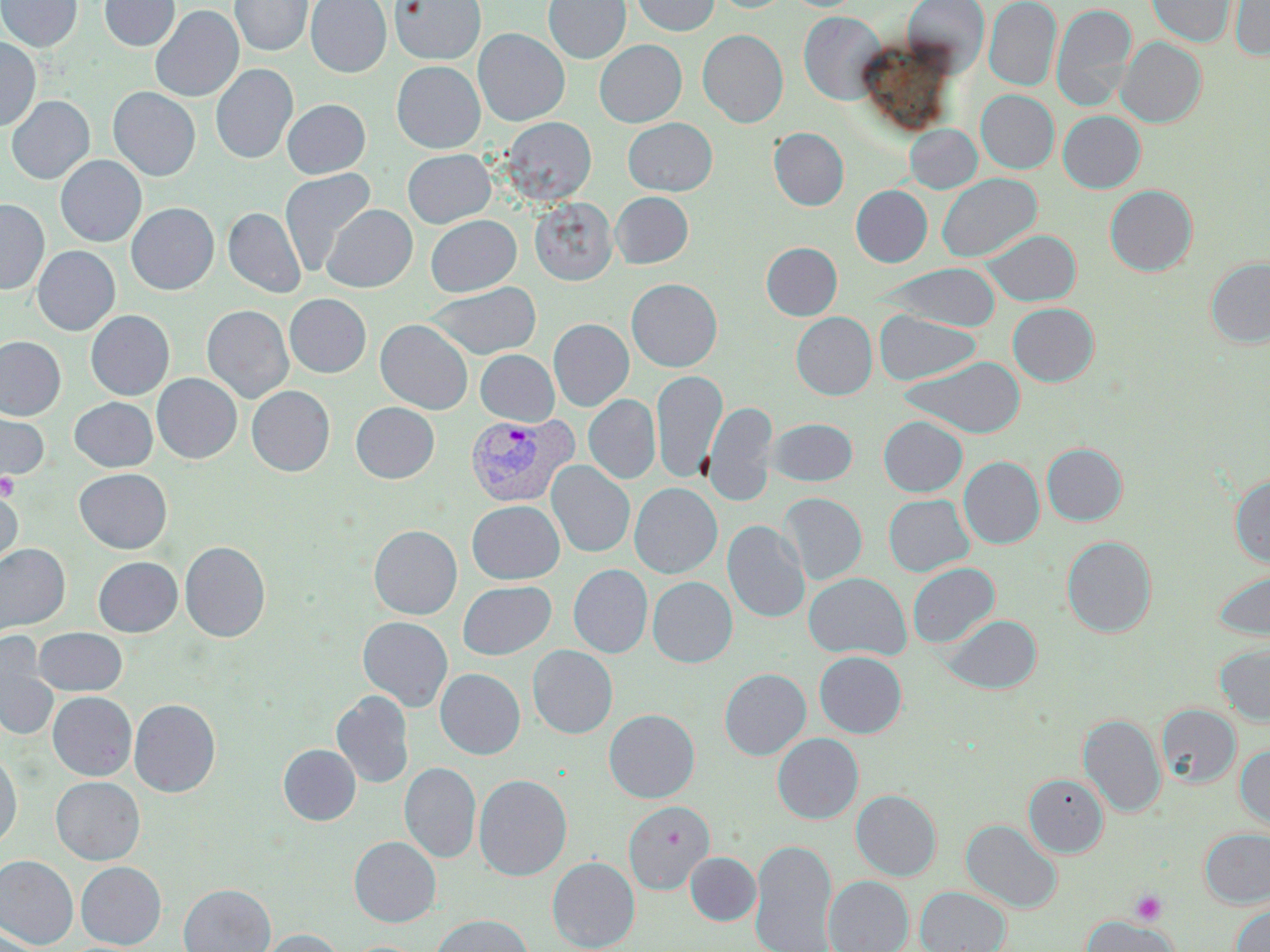
Approximate bounding boxes as (x1, y1, x2, y2) in pixels. Plasmodium vivax-infected red blood cell locations: (465, 414, 578, 508). Platelet locations: (0, 472, 20, 500), (1128, 889, 1169, 926). Uninfected red blood cell locations: (0, 0, 82, 52), (99, 0, 180, 51), (230, 0, 312, 56), (306, 0, 391, 77), (390, 0, 485, 65), (544, 0, 631, 64), (631, 0, 718, 35), (711, 0, 793, 13), (903, 0, 989, 73), (984, 0, 1061, 90), (1146, 0, 1237, 47), (1230, 1, 1270, 60), (1052, 3, 1137, 109), (150, 6, 243, 102), (798, 11, 887, 105), (473, 28, 569, 126), (698, 29, 788, 127), (0, 37, 41, 131), (1117, 37, 1206, 127), (594, 39, 687, 127), (392, 61, 485, 153), (211, 63, 298, 164), (108, 87, 200, 181), (976, 90, 1059, 173), (7, 96, 94, 184), (282, 99, 370, 178), (1058, 110, 1145, 192), (501, 116, 596, 205), (623, 118, 718, 195), (905, 124, 982, 193), (769, 128, 849, 210), (403, 149, 495, 227), (55, 155, 146, 246), (279, 168, 376, 276), (937, 173, 1042, 262), (851, 185, 932, 267), (1105, 185, 1197, 276), (611, 191, 693, 268), (529, 197, 618, 285), (0, 199, 50, 294), (126, 203, 219, 294), (321, 204, 417, 292), (223, 207, 306, 298), (426, 215, 521, 296), (983, 229, 1081, 306), (761, 242, 842, 320), (32, 246, 120, 335), (1206, 257, 1270, 347), (877, 263, 1001, 332), (626, 278, 722, 371), (424, 282, 541, 360), (284, 294, 371, 378), (1008, 303, 1098, 386), (202, 305, 294, 403), (86, 310, 175, 399), (875, 310, 981, 385), (791, 312, 877, 400), (549, 318, 634, 411), (375, 319, 473, 414), (0, 336, 66, 420), (475, 350, 559, 425), (901, 356, 1025, 437), (651, 369, 726, 484), (152, 373, 242, 463), (247, 385, 335, 476), (584, 395, 661, 483), (69, 397, 158, 471), (704, 400, 777, 507), (351, 402, 439, 483), (0, 406, 50, 487), (878, 416, 968, 496), (768, 417, 857, 486), (1042, 443, 1127, 525), (959, 456, 1044, 548), (547, 460, 635, 558), (74, 468, 172, 553), (1230, 474, 1270, 567), (629, 483, 722, 578), (0, 488, 23, 575), (779, 492, 867, 586), (884, 494, 974, 576), (467, 500, 564, 584), (723, 520, 810, 623), (369, 524, 462, 619), (1062, 536, 1156, 637), (179, 540, 271, 642), (0, 543, 70, 635), (93, 556, 182, 636), (907, 562, 1000, 648), (568, 564, 653, 658), (1212, 570, 1270, 640), (804, 572, 911, 660), (648, 577, 737, 667), (457, 580, 556, 659), (941, 615, 1042, 694), (358, 616, 453, 711), (34, 627, 127, 696), (0, 635, 59, 741), (1215, 643, 1270, 727), (528, 645, 618, 738), (814, 651, 907, 738), (435, 668, 525, 759), (719, 668, 811, 760), (331, 690, 414, 788), (47, 691, 136, 781), (129, 699, 221, 797), (1157, 704, 1241, 788), (604, 709, 700, 802), (1078, 714, 1165, 816), (772, 733, 863, 823), (278, 744, 360, 825), (1235, 746, 1270, 831), (0, 752, 22, 848), (400, 762, 481, 862), (1023, 773, 1108, 857), (473, 774, 572, 880), (51, 776, 145, 865), (59, 777, 152, 948), (851, 790, 941, 880), (623, 801, 715, 894), (962, 820, 1062, 914), (1200, 828, 1270, 908), (349, 836, 441, 927), (749, 838, 838, 952), (685, 852, 761, 925), (0, 855, 79, 949), (547, 857, 640, 952), (76, 861, 166, 949), (824, 876, 914, 952), (179, 883, 275, 952), (915, 886, 1011, 952), (1231, 903, 1270, 952), (430, 914, 533, 952), (1081, 916, 1178, 952), (0, 925, 43, 952), (256, 928, 346, 952). Slide-level diagnosis: Plasmodium vivax. Image is 1270×952 pixels. May-Grünwald-Giemsa stain. 1000x magnification. One field of a larger specimen. Thin blood film. Light microscopy.